Identify the parasite.
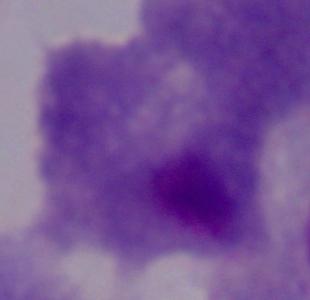

This is a trichomonad.

modality = micrograph
magnification = 1000x